Name the blood parasite species.
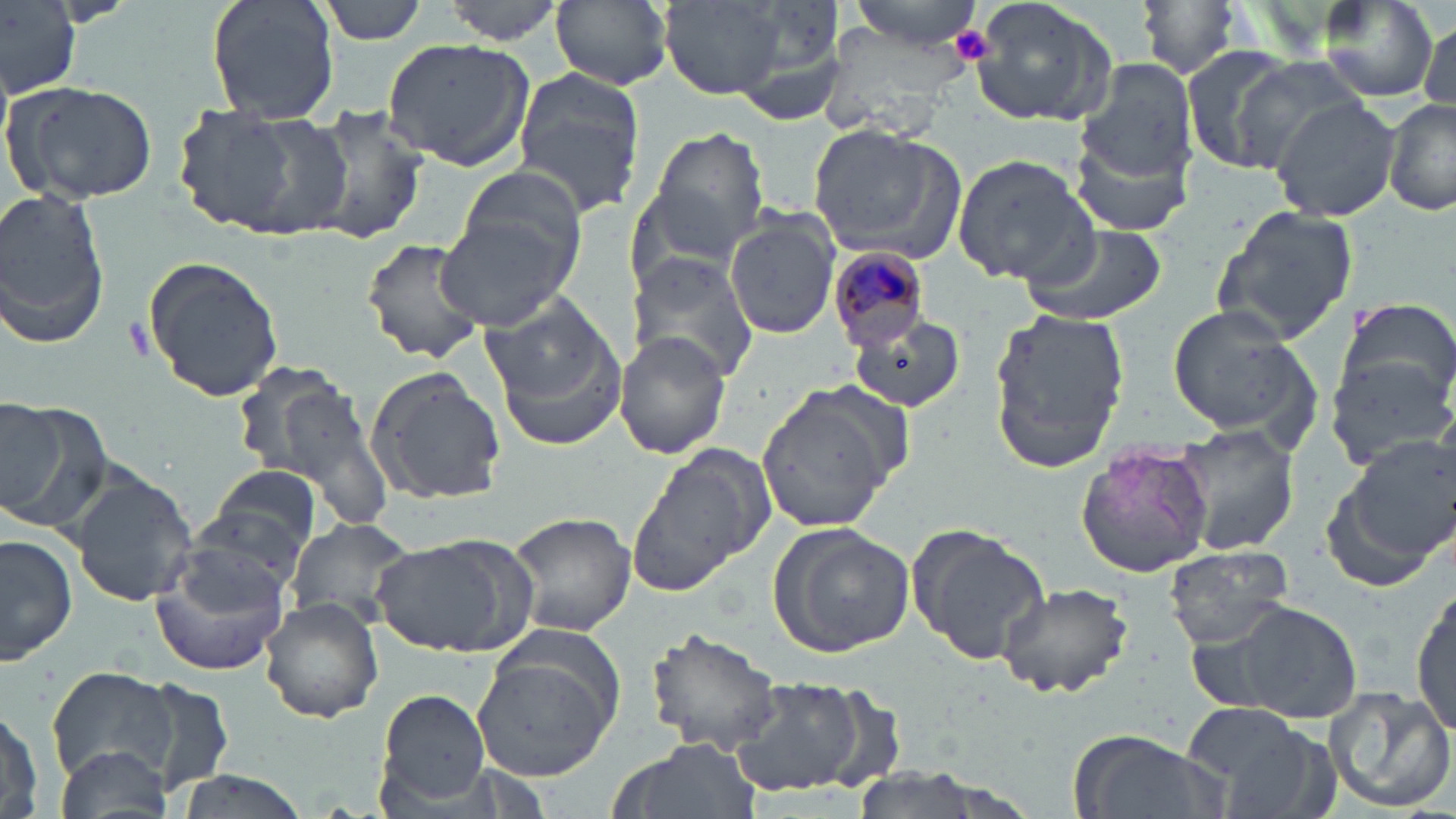
Plasmodium malariae.

image size = 1456×819 pixels
magnification = 1000x
preparation = thin blood smear
Plasmodium malariae-infected red blood cell locations = approximate bounding boxes as (x1, y1, x2, y2) in pixels: (828, 247, 932, 352)
field of view = one of a larger specimen
uninfected red blood cell locations = approximate bounding boxes as (x1, y1, x2, y2) in pixels: (205, 0, 340, 118), (314, 0, 432, 44), (441, 0, 565, 45), (551, 0, 674, 90), (662, 0, 788, 100), (841, 0, 991, 55), (968, 0, 1122, 129), (0, 1, 79, 100), (1134, 1, 1245, 83), (1315, 2, 1440, 103), (1419, 19, 1452, 116), (380, 38, 537, 172), (1180, 44, 1303, 174), (1234, 56, 1374, 164), (1079, 63, 1200, 187), (511, 65, 645, 219), (3, 81, 158, 207), (1272, 97, 1400, 223), (1384, 97, 1456, 219), (304, 104, 431, 248), (174, 107, 346, 242), (805, 123, 962, 260), (641, 125, 773, 260), (950, 154, 1097, 286), (453, 163, 588, 288), (0, 184, 112, 351), (1207, 205, 1362, 344), (435, 211, 580, 329), (723, 211, 841, 341), (1019, 221, 1168, 327), (361, 238, 485, 364), (628, 250, 763, 385), (142, 256, 284, 403), (480, 296, 629, 447), (1332, 298, 1456, 411), (1165, 302, 1319, 443), (987, 306, 1131, 476), (846, 313, 968, 413), (616, 331, 733, 460), (1324, 356, 1454, 471), (366, 367, 508, 504), (256, 373, 394, 522), (756, 387, 897, 536), (0, 399, 109, 532), (1171, 425, 1301, 555), (1322, 435, 1455, 588), (1074, 440, 1215, 581), (628, 449, 766, 589), (206, 462, 325, 565), (71, 472, 197, 607), (507, 510, 635, 638), (286, 517, 416, 632), (768, 522, 917, 657), (907, 524, 1052, 665), (0, 533, 77, 668), (373, 538, 531, 661), (150, 544, 292, 676), (1163, 544, 1296, 650), (996, 580, 1137, 700), (1412, 590, 1455, 744), (259, 597, 384, 722), (1219, 599, 1363, 723), (469, 626, 626, 784), (645, 627, 785, 758), (49, 665, 178, 788), (724, 676, 873, 796), (140, 679, 235, 796), (1320, 682, 1454, 815), (375, 688, 493, 810), (0, 700, 49, 818), (1183, 700, 1309, 794), (1216, 719, 1340, 819), (1071, 729, 1222, 819), (609, 737, 764, 819), (53, 743, 173, 819), (169, 770, 310, 819)
platelet locations = approximate bounding boxes as (x1, y1, x2, y2) in pixels: (951, 29, 994, 64)
stain = May-Grünwald-Giemsa
modality = light microscopy